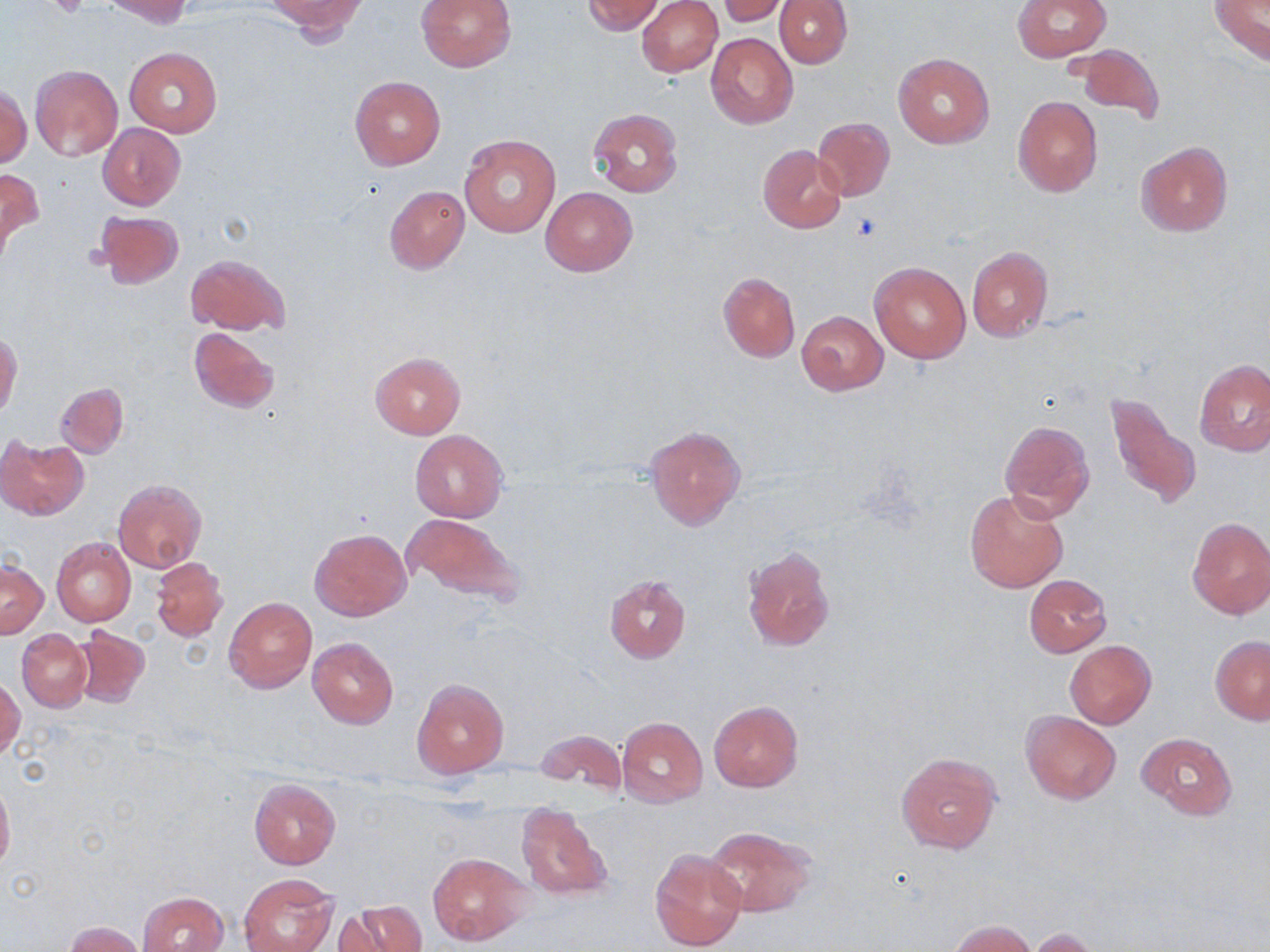

Summary:
  - Coordinate format: approximate bounding boxes as (x1, y1, x2, y2) in pixels
  - Platelet locations: (47, 0, 92, 20)
  - Uninfected red blood cell locations: (101, 0, 192, 27), (268, 0, 367, 40), (417, 0, 516, 72), (581, 0, 665, 35), (637, 0, 722, 76), (775, 0, 852, 68), (1013, 0, 1111, 62), (1209, 0, 1270, 65), (718, 1, 789, 26), (706, 32, 798, 130), (1071, 40, 1164, 124), (124, 47, 222, 136), (893, 52, 994, 149), (29, 65, 123, 161), (350, 76, 446, 170), (1, 86, 30, 169), (1012, 96, 1102, 197), (587, 108, 683, 199), (812, 117, 895, 203), (98, 123, 185, 210), (459, 135, 561, 238), (1136, 140, 1233, 236), (758, 146, 846, 233), (0, 166, 42, 258), (383, 186, 469, 274), (541, 187, 637, 277), (94, 210, 185, 289), (966, 245, 1054, 343), (187, 254, 289, 335), (868, 262, 970, 364), (717, 272, 800, 362), (797, 311, 888, 394), (189, 327, 281, 413), (0, 332, 21, 420), (370, 350, 465, 438), (1193, 359, 1270, 456), (55, 382, 129, 458), (1105, 390, 1200, 511), (997, 420, 1095, 522), (645, 424, 745, 530), (410, 430, 508, 521), (0, 435, 88, 519), (113, 480, 206, 571), (964, 488, 1068, 593), (404, 513, 524, 605), (1186, 517, 1270, 620), (310, 528, 410, 620), (51, 537, 135, 626), (741, 546, 835, 652), (150, 556, 228, 643), (1, 559, 47, 638), (605, 575, 692, 663), (1023, 575, 1111, 657), (224, 596, 317, 693), (72, 626, 151, 707), (16, 629, 92, 714), (1211, 634, 1270, 723), (307, 636, 398, 729), (1065, 641, 1155, 728), (1, 676, 23, 759), (412, 678, 509, 777), (709, 700, 803, 792), (1021, 710, 1121, 804), (616, 717, 708, 808), (534, 729, 627, 797), (1138, 731, 1238, 820), (896, 749, 1002, 853), (250, 778, 342, 869), (0, 781, 14, 874), (515, 800, 613, 903), (704, 825, 814, 918), (648, 848, 746, 951), (428, 852, 531, 946), (240, 873, 338, 952), (137, 891, 231, 952), (337, 900, 424, 952), (949, 919, 1036, 951), (63, 920, 145, 952), (1026, 928, 1105, 952)
  - Slide-level diagnosis: no evidence of blood parasites
  - Stain: May-Grünwald-Giemsa
  - Magnification: 1000x
  - Modality: optical microscopy
  - Image size: 1270×952 pixels
  - Field of view: one of a larger specimen
  - Preparation: thin blood smear